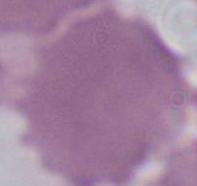
An erythrocyte is shown. Captured at 1000x magnification. Photomicrograph.